Identify the blood parasite species.
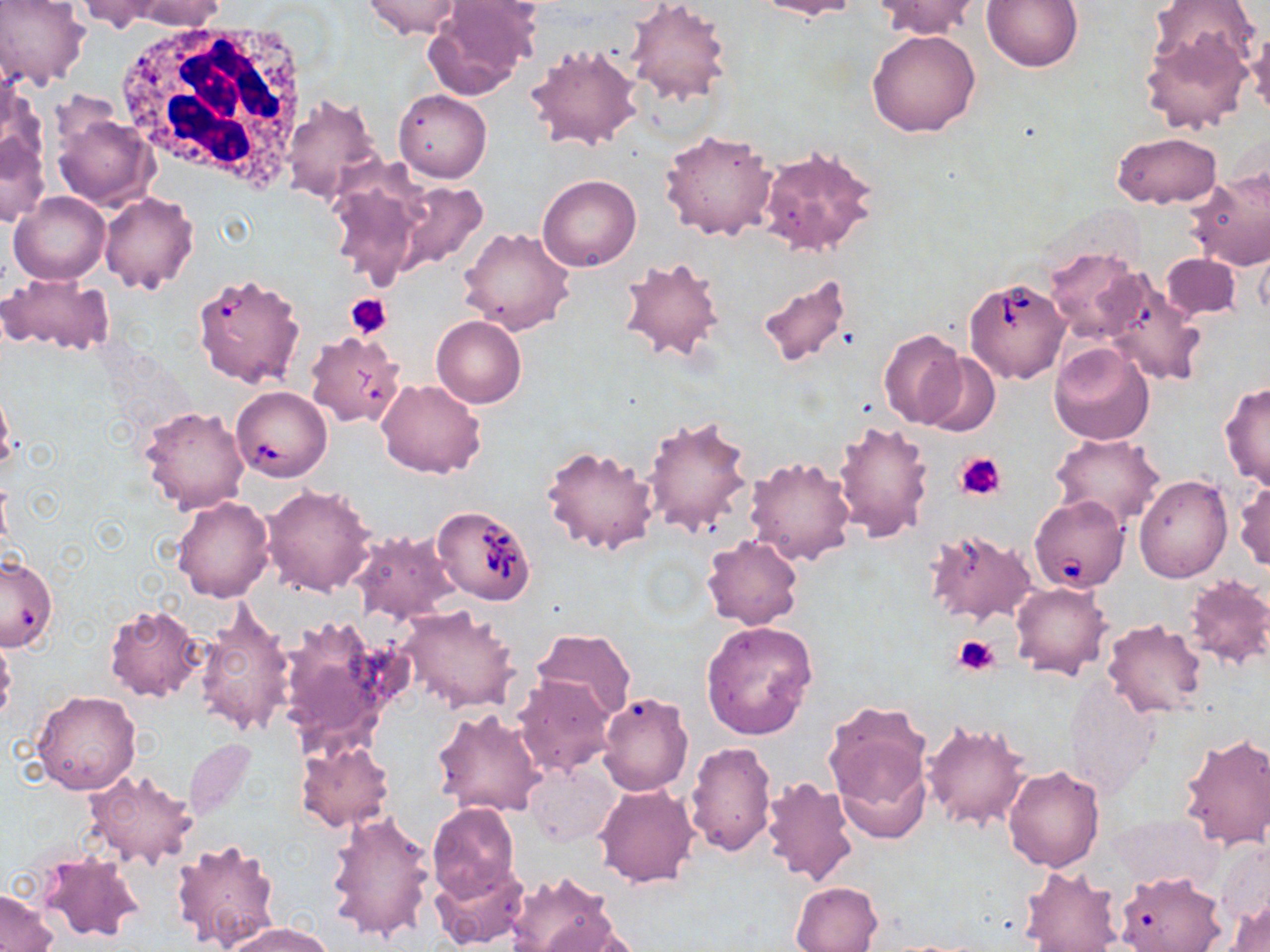

Babesia divergens.

Approximate bounding boxes as [x1, y1, x2, y2] in pixels. Platelet locations: [346, 293, 392, 338], [957, 452, 1006, 502], [954, 635, 1000, 675]. Uninfected red blood cell locations: [71, 0, 169, 33], [116, 0, 227, 30], [361, 0, 464, 39], [624, 0, 732, 108], [753, 0, 860, 20], [876, 0, 980, 39], [982, 0, 1085, 73], [1149, 0, 1259, 74], [0, 1, 91, 91], [422, 1, 540, 99], [1245, 23, 1270, 115], [867, 28, 981, 138], [1140, 29, 1253, 134], [526, 42, 645, 152], [1, 82, 48, 190], [393, 89, 491, 182], [282, 94, 383, 206], [50, 111, 158, 210], [660, 128, 779, 240], [0, 129, 51, 229], [1112, 131, 1222, 208], [758, 144, 878, 259], [323, 162, 428, 286], [1185, 170, 1270, 271], [537, 175, 641, 271], [392, 183, 491, 276], [9, 191, 110, 284], [100, 192, 200, 294], [458, 227, 575, 336], [1044, 248, 1145, 343], [616, 253, 728, 365], [1161, 253, 1241, 320], [754, 272, 858, 369], [0, 273, 113, 355], [1098, 275, 1205, 388], [432, 315, 526, 407], [878, 329, 966, 429], [1049, 342, 1156, 444], [918, 352, 1001, 437], [377, 378, 488, 479], [0, 379, 14, 474], [1219, 380, 1270, 490], [139, 405, 250, 514], [642, 415, 754, 537], [833, 419, 933, 544], [1050, 433, 1165, 529], [541, 445, 661, 557], [744, 455, 857, 567], [1134, 476, 1231, 581], [1233, 477, 1270, 573], [261, 483, 378, 596], [170, 496, 274, 603], [925, 528, 1036, 626], [349, 529, 461, 627], [702, 533, 802, 629], [1180, 574, 1270, 670], [1011, 582, 1111, 681], [195, 602, 296, 738], [103, 604, 205, 702], [398, 606, 521, 713], [277, 611, 409, 755], [700, 619, 817, 739], [1102, 619, 1207, 718], [531, 627, 637, 721], [0, 633, 16, 729], [512, 674, 617, 779], [1063, 677, 1163, 797], [32, 689, 142, 796], [597, 692, 693, 795], [822, 700, 935, 836], [432, 708, 548, 817], [922, 719, 1033, 832], [1179, 733, 1270, 851], [184, 738, 258, 821], [294, 740, 397, 833], [686, 740, 776, 857], [524, 761, 619, 847], [1004, 765, 1106, 872], [85, 769, 199, 870], [758, 777, 858, 888], [595, 784, 699, 887], [426, 803, 519, 900], [325, 810, 437, 945], [170, 838, 283, 952], [34, 850, 144, 946], [431, 860, 531, 950], [1018, 865, 1122, 951], [504, 870, 617, 952], [1114, 870, 1227, 952], [791, 881, 882, 951], [0, 890, 57, 950], [1227, 898, 1270, 951], [544, 917, 643, 951], [225, 921, 332, 952]. Babesia divergens-infected red blood cell locations: [191, 272, 305, 387], [964, 276, 1070, 385], [305, 331, 405, 428], [232, 386, 332, 482], [1029, 494, 1130, 593], [431, 505, 537, 605], [0, 553, 56, 651]. White blood cell locations: [113, 17, 311, 194]. May-Grünwald-Giemsa-stained preparation. Light microscopy. One field of a larger specimen. Thin blood film. 1000x magnification. Image is 1270×952 pixels.